Comment on the morphology of the red blood cells.
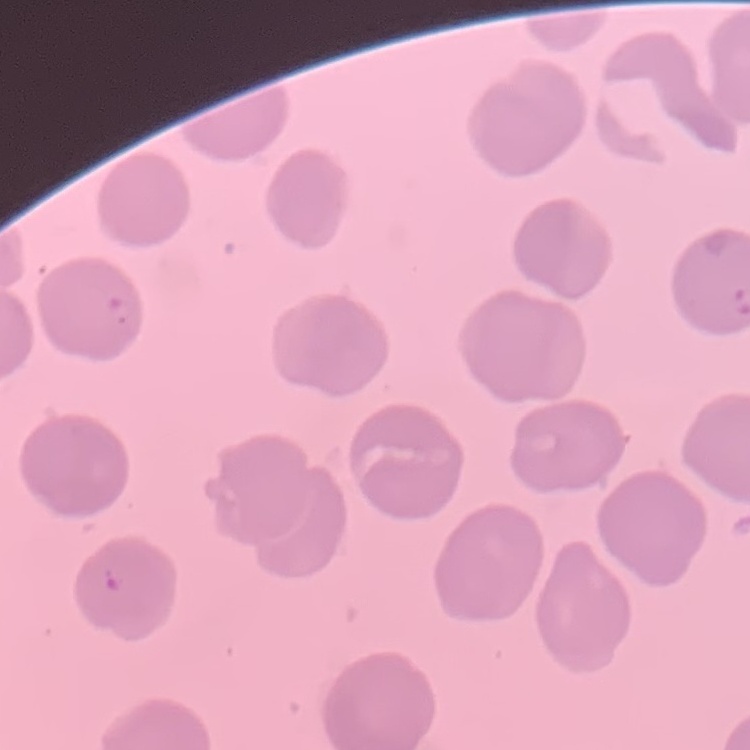

No rouleaux formation.

preparation: thin blood smear
image_type: square crop of a larger photomicrograph
stain: Field's or Giemsa